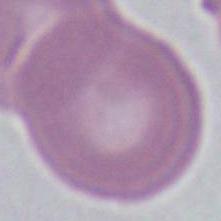
Summary:
  - Modality: photomicrograph
  - Identification: erythrocyte
  - Magnification: 1000x